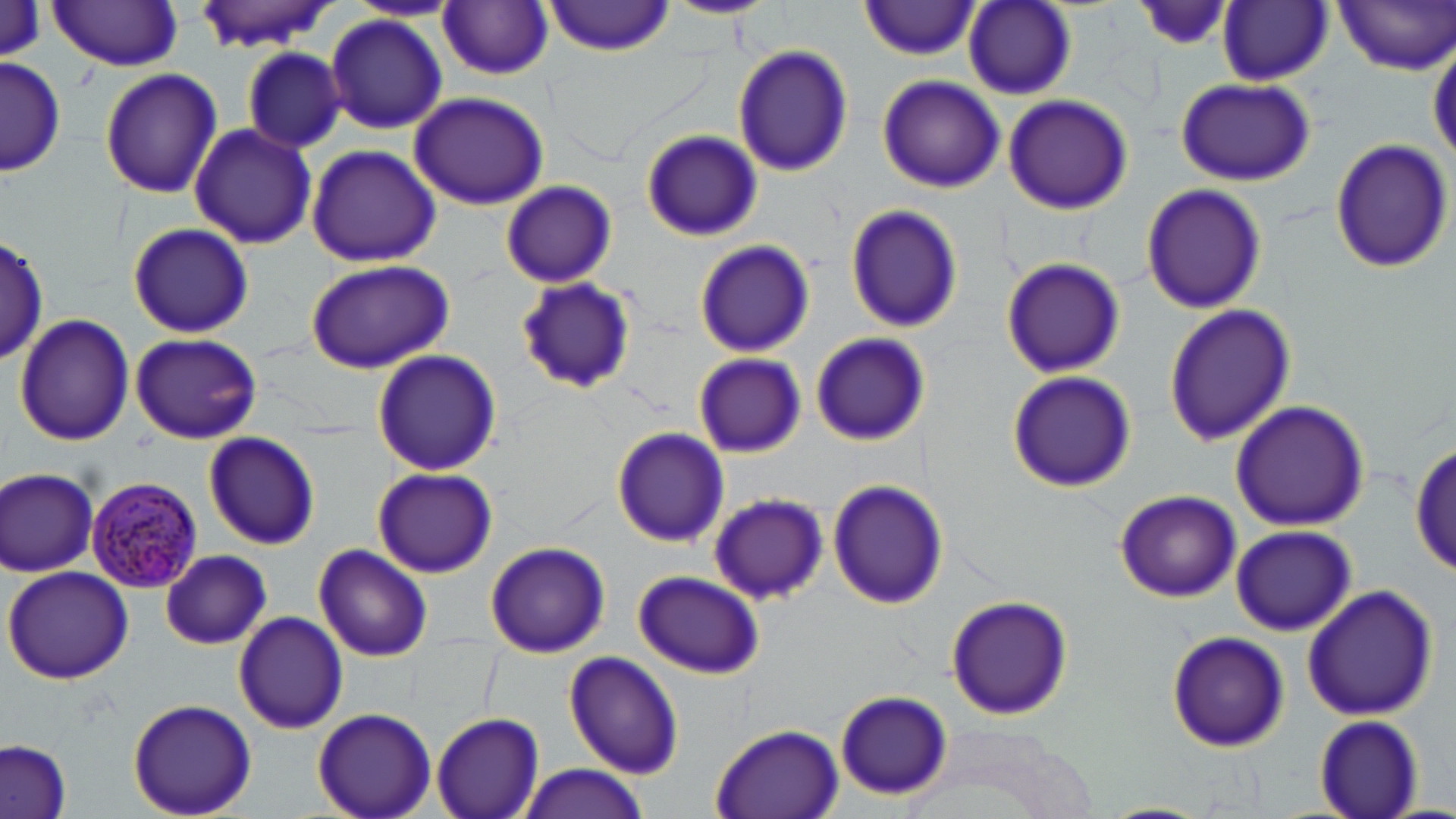

Approximate bounding boxes as (x1,y1)-(x2,y2) corner pairs in pixels. Plasmodium malariae-infected red blood cell locations: (87,476)-(203,593). Uninfected red blood cell locations: (192,0)-(343,52), (663,0)-(773,19), (1130,0)-(1232,51), (1218,0)-(1332,85), (1335,0)-(1456,74), (349,1)-(462,22), (546,1)-(672,56), (860,1)-(981,59), (47,2)-(184,70), (439,2)-(553,80), (963,2)-(1076,101), (325,13)-(447,135), (1429,38)-(1456,167), (732,44)-(854,178), (241,46)-(346,153), (2,58)-(65,178), (98,67)-(223,199), (877,74)-(1004,193), (1173,75)-(1315,185), (408,92)-(550,210), (1003,95)-(1134,215), (187,121)-(317,250), (640,128)-(762,241), (1329,138)-(1452,272), (306,144)-(443,267), (499,179)-(618,289), (1141,183)-(1268,314), (844,202)-(962,334), (126,221)-(254,339), (1,233)-(49,367), (693,238)-(813,359), (999,256)-(1125,378), (303,259)-(454,375), (514,276)-(636,397), (1163,304)-(1294,448), (13,314)-(135,447), (808,331)-(929,444), (129,333)-(262,444), (372,350)-(501,476), (691,351)-(808,458), (1006,370)-(1137,493), (1230,400)-(1370,530), (612,426)-(729,547), (202,431)-(321,550), (1412,444)-(1454,574), (372,466)-(497,578), (1,468)-(99,576), (826,479)-(947,611), (1114,489)-(1242,602), (708,492)-(829,605), (1231,524)-(1356,636), (484,541)-(610,659), (313,545)-(431,661), (161,551)-(272,651), (3,566)-(133,684), (633,572)-(764,679), (1302,584)-(1439,722), (944,594)-(1074,721), (233,611)-(348,732), (1166,629)-(1290,754), (563,651)-(685,777), (834,691)-(952,799), (126,699)-(257,818), (311,706)-(436,818), (430,712)-(544,819), (1313,712)-(1427,818), (708,722)-(844,819), (1,741)-(73,819), (516,763)-(652,818), (1101,802)-(1214,819). Slide-level diagnosis: Plasmodium malariae. Optical microscopy. Captured at 1000x magnification. Single field of view. Thin blood film. May-Grünwald-Giemsa stain. Image is 1456×819 pixels.